Point out every malaria parasite and every leukocyte.
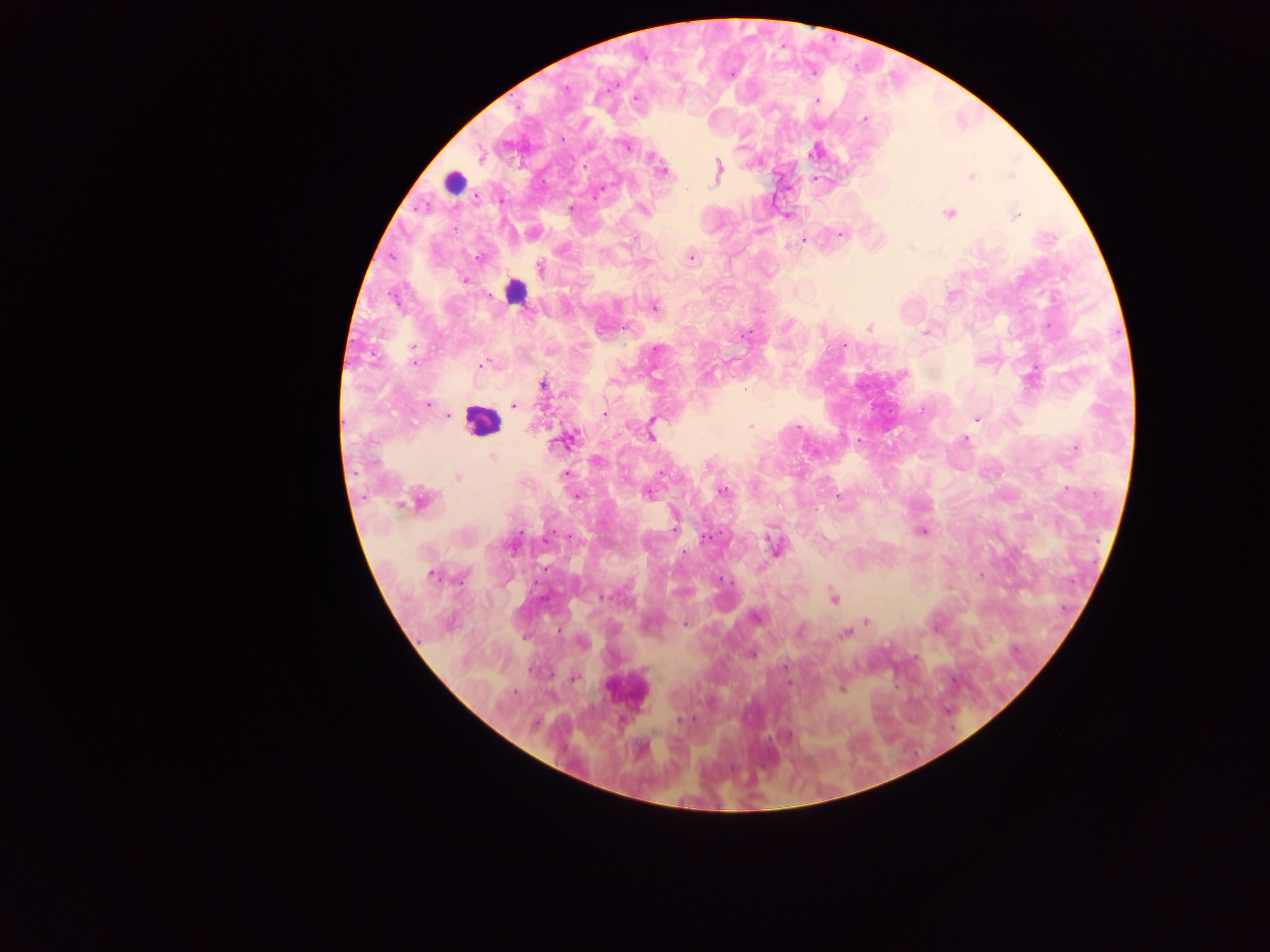

Approximate centers as {x, y} in pixels.
Malaria parasites: {616, 84}, {565, 88}, {636, 98}, {817, 101}, {864, 119}, {562, 139}, {626, 145}, {481, 156}, {718, 169}, {663, 171}, {1012, 176}, {971, 177}, {600, 190}, {571, 207}, {642, 210}, {948, 213}, {1015, 215}, {840, 234}, {803, 241}, {691, 257}, {477, 258}, {540, 268}, {465, 280}, {616, 304}, {654, 307}, {869, 327}, {925, 333}, {743, 335}, {844, 345}, {414, 348}, {657, 349}, {415, 362}, {482, 365}, {657, 380}, {612, 381}, {544, 385}, {428, 405}, {514, 405}, {604, 413}, {449, 416}, {976, 419}, {653, 422}, {750, 426}, {798, 427}, {651, 435}, {965, 440}, {564, 441}, {1075, 448}, {493, 457}, {597, 461}, {565, 474}, {661, 474}, {458, 477}, {722, 491}, {648, 494}, {576, 496}, {839, 496}, {422, 500}, {674, 528}, {922, 531}, {569, 536}, {705, 538}, {546, 539}, {774, 546}, {685, 553}, {431, 576}, {604, 597}, {833, 598}, {756, 617}, {866, 620}, {685, 625}, {799, 632}, {844, 633}, {581, 643}, {751, 654}, {785, 667}, {575, 678}, {788, 683}, {514, 691}, {681, 720}, {789, 736}, {641, 748}.
Leukocytes: {453, 182}, {516, 291}, {480, 420}.

capture = mobile-phone photograph through a microscope
field of view = single
country = Ghana
preparation = thick blood film
image size = 1270×952 pixels